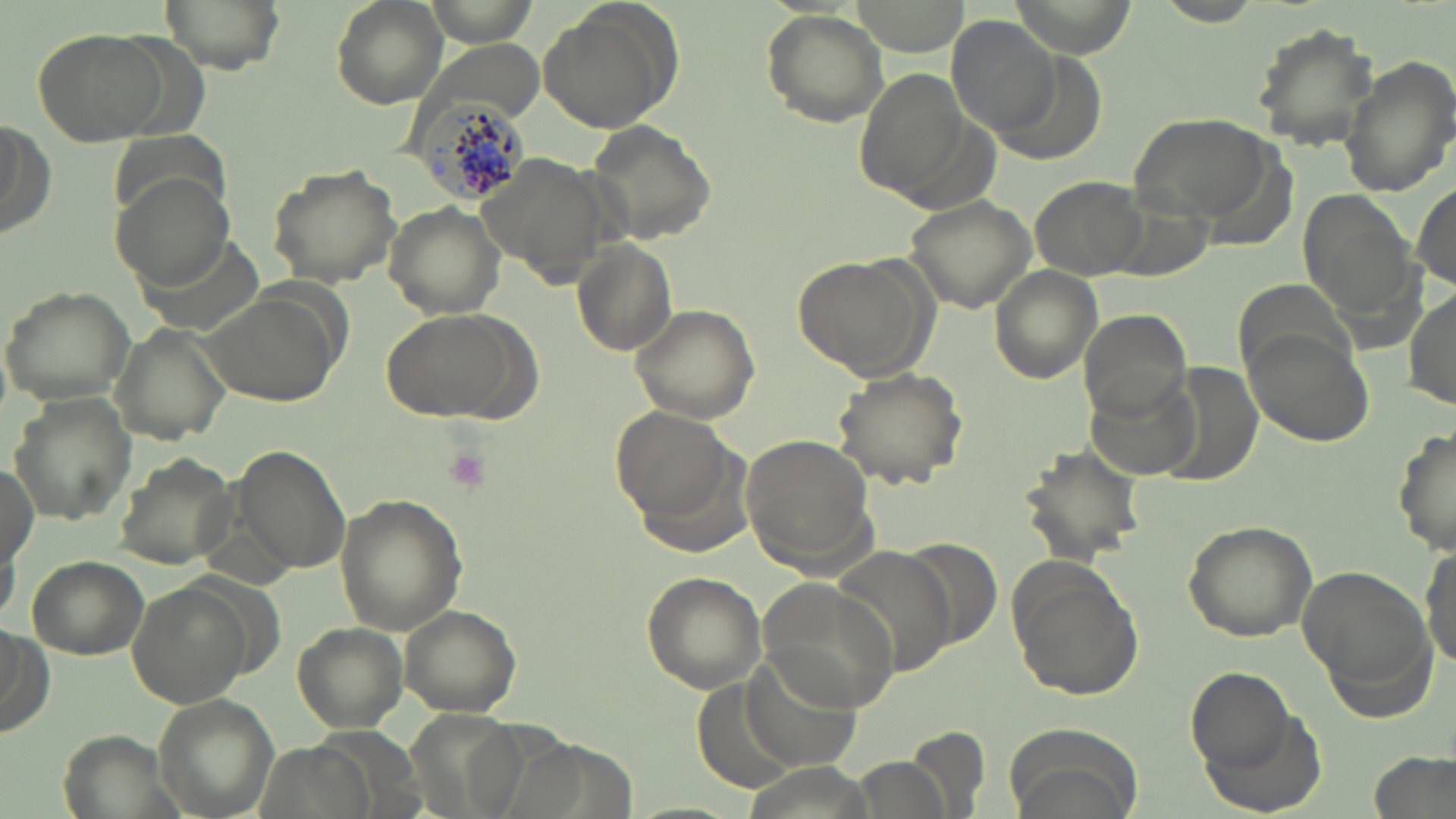
Approximate bounding boxes as named x1/y1/x2/y2 corners in pixels. Platelet locations: (x1=440, y1=446, x2=493, y2=495). Uninfected red blood cell locations: (x1=157, y1=0, x2=287, y2=73), (x1=332, y1=0, x2=448, y2=109), (x1=422, y1=0, x2=543, y2=47), (x1=1153, y1=2, x2=1265, y2=28), (x1=536, y1=4, x2=677, y2=135), (x1=761, y1=8, x2=889, y2=127), (x1=947, y1=14, x2=1059, y2=138), (x1=1252, y1=23, x2=1379, y2=149), (x1=32, y1=28, x2=168, y2=146), (x1=1341, y1=56, x2=1456, y2=198), (x1=1130, y1=110, x2=1277, y2=223), (x1=0, y1=115, x2=53, y2=243), (x1=585, y1=119, x2=719, y2=247), (x1=263, y1=163, x2=401, y2=288), (x1=112, y1=171, x2=237, y2=291), (x1=1029, y1=174, x2=1150, y2=280), (x1=1411, y1=182, x2=1456, y2=292), (x1=1296, y1=187, x2=1419, y2=326), (x1=902, y1=194, x2=1039, y2=315), (x1=382, y1=202, x2=506, y2=320), (x1=573, y1=239, x2=679, y2=356), (x1=795, y1=254, x2=936, y2=383), (x1=989, y1=266, x2=1101, y2=383), (x1=1235, y1=279, x2=1355, y2=384), (x1=1, y1=285, x2=136, y2=406), (x1=201, y1=286, x2=344, y2=405), (x1=1407, y1=286, x2=1455, y2=412), (x1=628, y1=302, x2=760, y2=425), (x1=379, y1=306, x2=540, y2=423), (x1=1076, y1=308, x2=1193, y2=422), (x1=110, y1=323, x2=233, y2=444), (x1=1242, y1=331, x2=1374, y2=446), (x1=830, y1=365, x2=967, y2=488), (x1=1160, y1=365, x2=1264, y2=486), (x1=1089, y1=379, x2=1197, y2=479), (x1=9, y1=392, x2=137, y2=524), (x1=609, y1=407, x2=737, y2=526), (x1=1394, y1=425, x2=1455, y2=559), (x1=742, y1=434, x2=878, y2=570), (x1=233, y1=445, x2=352, y2=575), (x1=1016, y1=445, x2=1148, y2=567), (x1=112, y1=452, x2=241, y2=568), (x1=0, y1=457, x2=38, y2=568), (x1=332, y1=493, x2=468, y2=634), (x1=1181, y1=518, x2=1318, y2=644), (x1=1419, y1=543, x2=1455, y2=670), (x1=25, y1=555, x2=148, y2=660), (x1=1005, y1=556, x2=1145, y2=702), (x1=1299, y1=563, x2=1433, y2=712), (x1=640, y1=571, x2=767, y2=693), (x1=757, y1=576, x2=898, y2=713), (x1=128, y1=582, x2=254, y2=709), (x1=399, y1=603, x2=524, y2=716), (x1=294, y1=623, x2=407, y2=731), (x1=0, y1=624, x2=50, y2=738), (x1=741, y1=655, x2=860, y2=772), (x1=1187, y1=665, x2=1295, y2=769), (x1=150, y1=693, x2=279, y2=819), (x1=1199, y1=711, x2=1326, y2=816), (x1=1006, y1=722, x2=1145, y2=819), (x1=907, y1=726, x2=994, y2=818), (x1=1369, y1=751, x2=1453, y2=819), (x1=855, y1=758, x2=950, y2=819). Plasmodium malariae-infected red blood cell locations: (x1=408, y1=92, x2=532, y2=206). Slide-level diagnosis: Plasmodium malariae. Thin blood smear. One field of a larger specimen. Optical microscopy. May-Grünwald-Giemsa stain. Image is 1456×819 pixels. Captured at 1000x magnification.